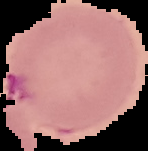

Summary:
  - Preparation: thin blood smear
  - Result: malaria parasites detected
  - Image type: segmented cell region on a black background
  - Image size: 148×151 pixels